Identify the parasite.
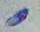
Toxoplasma gondii.

Summary:
  - Magnification: 1000x
  - Modality: micrograph